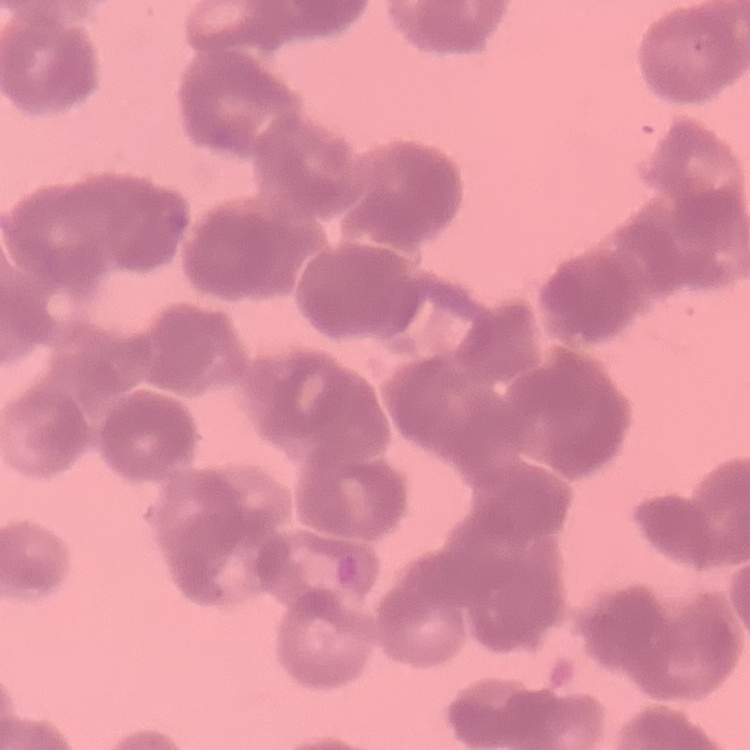
{
  "erythrocyte_morphology": "rouleaux formation",
  "image_type": "one tile cut from a larger photomicrograph",
  "preparation": "thin blood smear",
  "stain": "Field's or Giemsa"
}